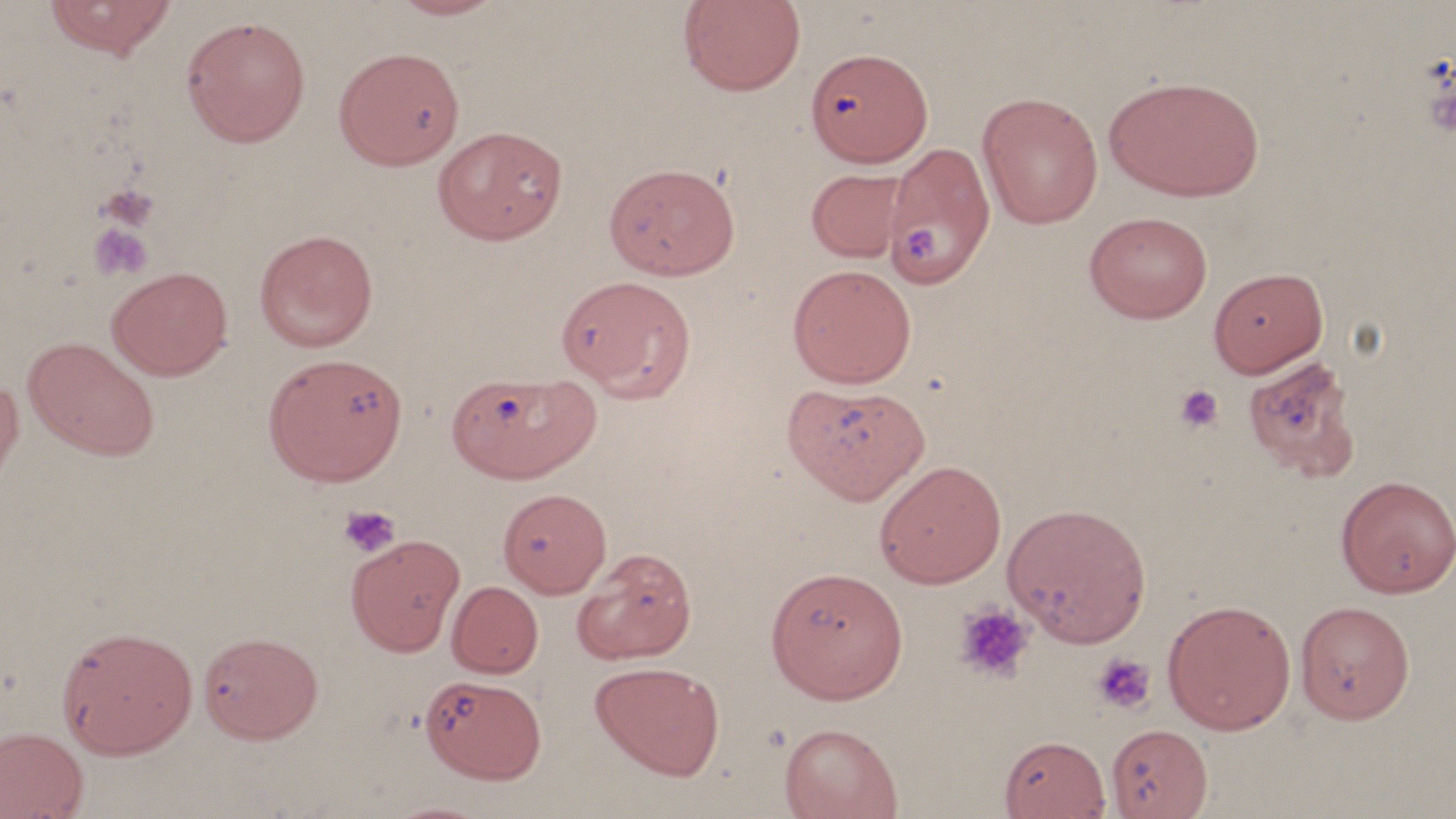
slide_level_diagnosis: negative for blood parasites
platelet_locations: 'approximate bounding boxes as (x1,y1)-(x2,y2) corner pairs in pixels: (98,182)-(160,230), (86,222)-(154,283), (906,224)-(942,263), (1175,385)-(1224,433), (338,504)-(401,558), (953,602)-(1035,684), (1092,652)-(1156,715)'
modality: optical microscopy
image_size: 1456×819 pixels
field_of_view: single
uninfected_red_blood_cell_locations: 'approximate bounding boxes as (x1,y1)-(x2,y2) corner pairs in pixels: (41,0)-(179,60), (384,0)-(510,20), (677,0)-(806,97), (180,14)-(311,148), (333,45)-(464,170), (806,47)-(932,165), (1104,75)-(1265,202), (976,92)-(1103,229), (432,125)-(567,245), (886,143)-(995,289), (604,163)-(740,281), (805,168)-(909,263), (1084,210)-(1213,324), (254,229)-(378,353), (787,264)-(917,388), (106,266)-(233,380), (1208,267)-(1328,378), (557,280)-(695,407), (22,336)-(162,462), (262,353)-(408,486), (1241,354)-(1360,482), (448,370)-(598,483), (0,375)-(23,496), (782,383)-(929,504), (873,460)-(1007,588), (1335,475)-(1456,598), (498,488)-(612,598), (1001,501)-(1152,648), (346,534)-(465,656), (571,548)-(697,664), (765,565)-(908,704), (447,581)-(543,678), (1161,599)-(1297,735), (1294,600)-(1415,724), (55,624)-(198,758), (197,630)-(324,744), (590,661)-(724,780), (420,674)-(547,784), (779,722)-(903,819), (1104,723)-(1213,818), (0,726)-(89,819), (999,734)-(1112,819), (380,798)-(498,819)'
magnification: 1000x
preparation: thin blood film
stain: May-Grünwald-Giemsa